Classify this cell by malaria status.
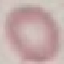

It is uninfected.

{
  "preparation": "thin blood smear",
  "image_type": "cell patch, automatically extracted from a larger field of view and resized to 64 × 64 pixels",
  "capture": "smartphone camera at the microscope eyepiece",
  "stain": "Giemsa"
}